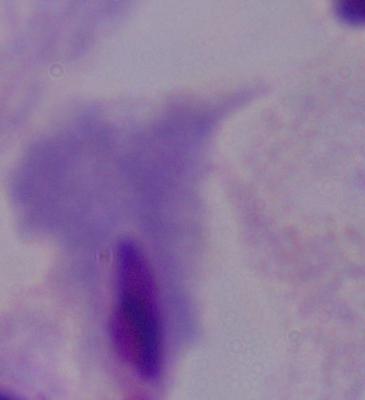
Photomicrograph. A trichomonad is seen. 1000x magnification.